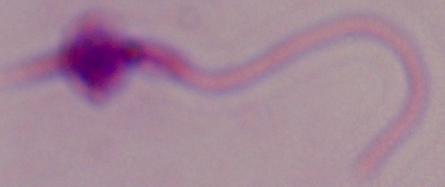

Summary:
  - Identification: Leishmania
  - Magnification: 1000x
  - Modality: photomicrograph